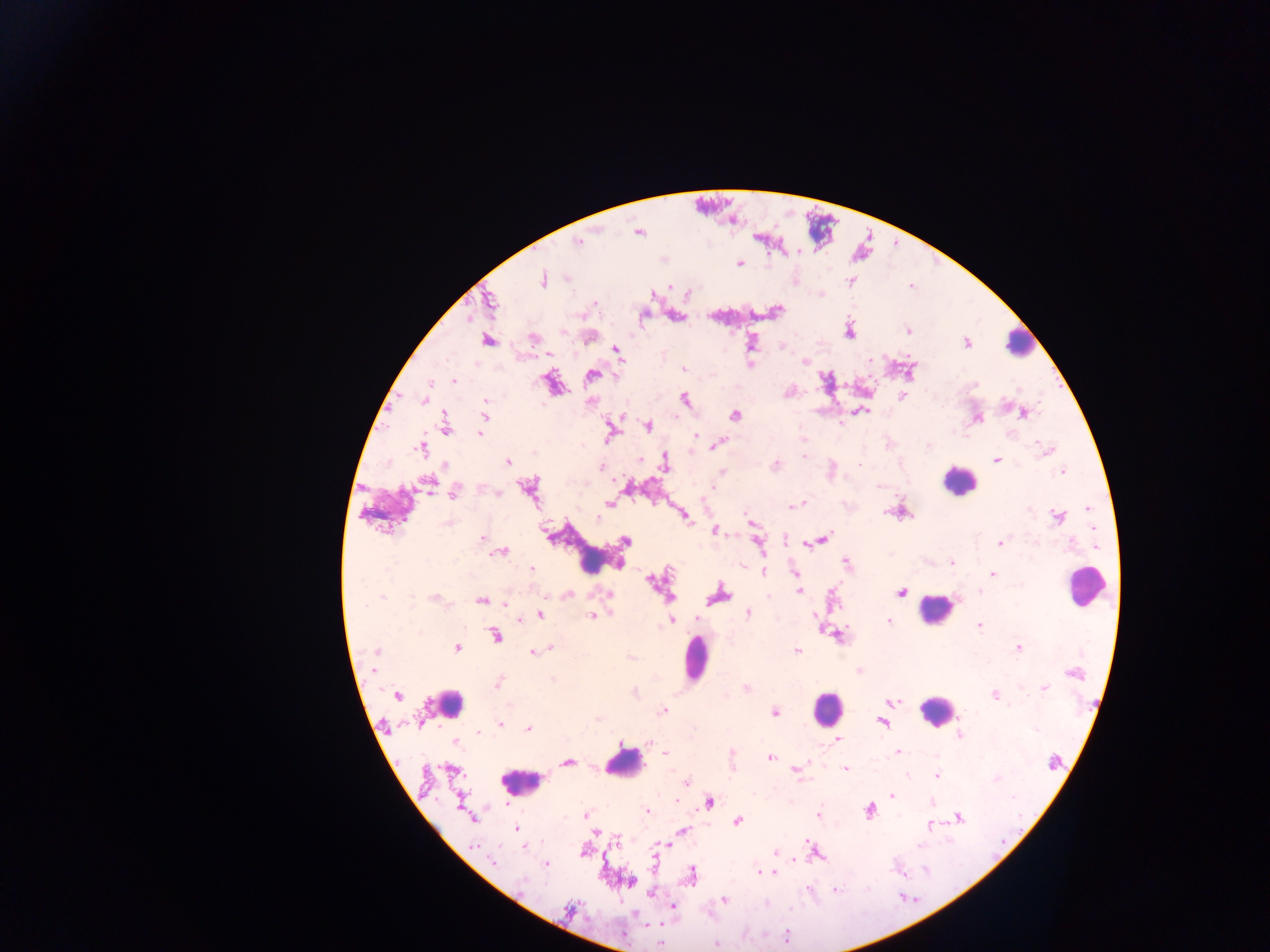
Approximate centers as [x, y] in pixels. Malaria parasite locations: [599, 230], [638, 234], [584, 241], [578, 242], [740, 263], [567, 279], [543, 281], [849, 282], [821, 296], [561, 331], [908, 332], [848, 334], [750, 340], [966, 343], [782, 347], [615, 350], [805, 360], [684, 369], [592, 373], [454, 381], [431, 383], [426, 395], [903, 396], [685, 398], [424, 401], [486, 411], [865, 412], [1023, 414], [735, 416], [982, 418], [445, 424], [612, 425], [649, 426], [608, 434], [695, 434], [481, 435], [698, 435], [803, 438], [721, 443], [1039, 444], [928, 447], [420, 449], [1042, 455], [803, 457], [639, 458], [997, 459], [508, 463], [444, 464], [776, 464], [859, 464], [664, 466], [601, 468], [1062, 471], [429, 482], [527, 487], [631, 488], [709, 490], [454, 493], [497, 493], [610, 503], [605, 505], [796, 505], [1089, 509], [889, 512], [684, 515], [1056, 517], [598, 519], [747, 519], [445, 523], [715, 531], [1093, 531], [482, 537], [825, 538], [1073, 539], [625, 542], [1000, 542], [759, 544], [806, 544], [1098, 545], [502, 551], [951, 562], [620, 563], [532, 568], [793, 569], [763, 571], [993, 575], [651, 580], [798, 592], [900, 592], [979, 592], [608, 593], [568, 595], [667, 597], [719, 597], [434, 598], [767, 598], [382, 599], [482, 599], [412, 600], [956, 600], [369, 604], [504, 605], [366, 606], [748, 612], [611, 613], [542, 614], [592, 615], [817, 615], [698, 618], [673, 620], [521, 621], [888, 621], [979, 624], [496, 635], [1020, 646], [456, 647], [551, 647], [377, 651], [542, 651], [797, 651], [534, 653], [375, 671], [553, 679], [493, 685], [1044, 686], [397, 694], [995, 695], [893, 701], [511, 703], [663, 710], [774, 712], [597, 718], [884, 724], [500, 725], [529, 729], [479, 732], [961, 734], [837, 741], [650, 745], [898, 751], [663, 752], [770, 756], [567, 761], [845, 767], [425, 771], [908, 774], [937, 774], [797, 776], [687, 781], [893, 796], [677, 800], [710, 801], [932, 802], [868, 812], [584, 813], [646, 813], [819, 813], [958, 817], [738, 821], [931, 824], [516, 829], [684, 830], [596, 833], [619, 838], [806, 841], [670, 844], [475, 845], [919, 847], [815, 850], [775, 852], [653, 856], [801, 860], [495, 862], [545, 865], [757, 870], [927, 871], [775, 873], [899, 873], [691, 874], [522, 880], [836, 891], [650, 894], [724, 899], [767, 903], [672, 907], [570, 910], [787, 935], [661, 944], [716, 944]. Leukocyte locations: [1020, 344], [954, 480], [579, 550], [1085, 581], [935, 607], [700, 659], [448, 702], [824, 705], [934, 706], [626, 762], [516, 779]. Sample from Ghana. Photographed through a microscope with a mobile-phone camera. Thick blood film. Single field of view. Image is 1270×952 pixels.